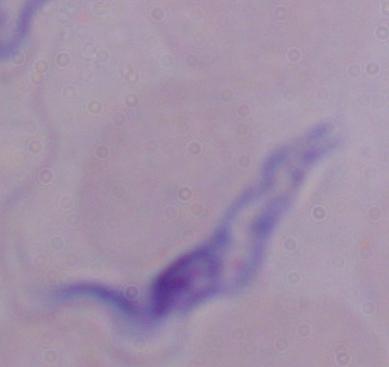

identification: trypanosome
modality: photomicrograph
magnification: 1000x